Assess this cell for malaria.
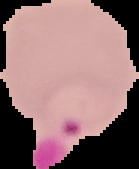
It is parasitized.

image_type: cell region segmented out of the field of view; surrounding area masked to black
image_size: 139×169 pixels
preparation: thin blood smear